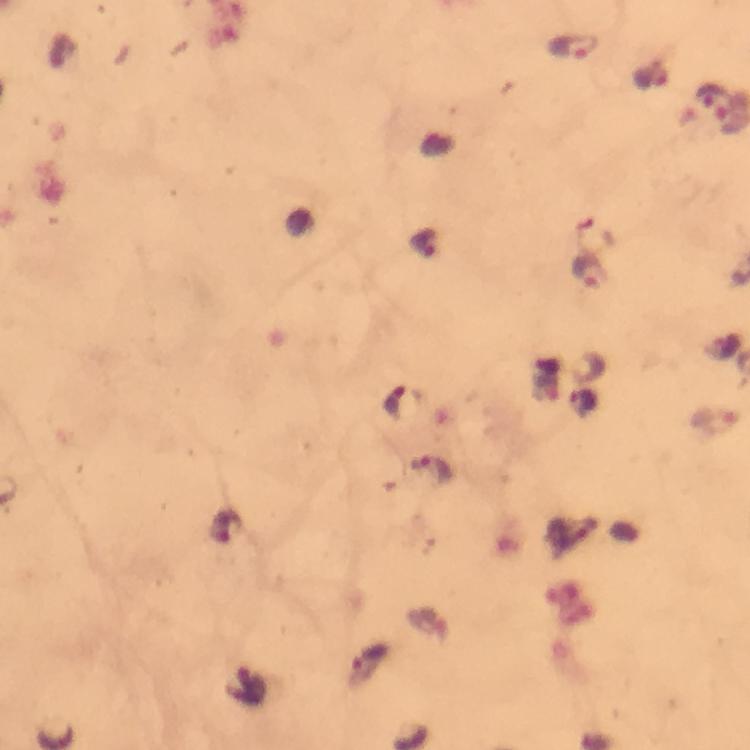 Approximate centers as [x, y] in pixels. Plasmodium parasite locations: [572, 46], [714, 102], [596, 235], [590, 272]. From a malaria diagnostic workup. At 100x magnification. A crop from one field of view. Thick blood film. Giemsa stain. Photographed through the microscope with a smartphone camera. Immersion oil was used. Image is 750×750 pixels.